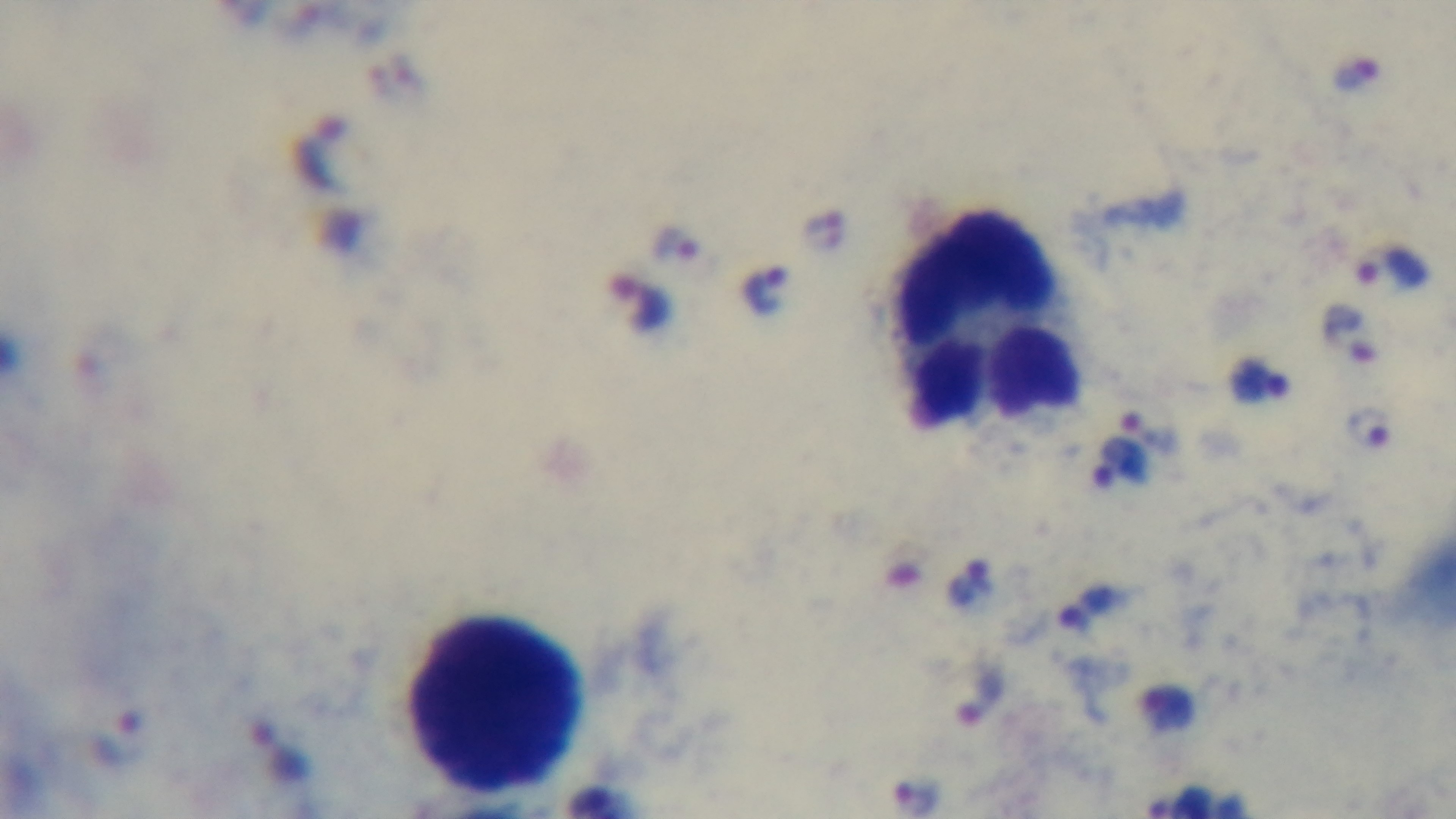
Summary:
  - Preparation: thick blood film
  - Objective: 100x oil immersion
  - Modality: light microscopy
  - Malaria status: positive
  - Stain: Giemsa
  - Field of view: one from the slide
  - Capture: mounted 4K digital camera